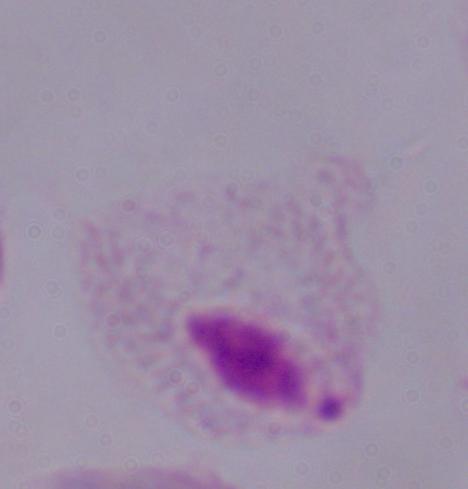

Photomicrograph. A trichomonad is shown. Captured at 1000x magnification.